State which cell type is depicted.
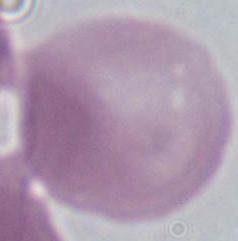
This is an erythrocyte.

Captured at 1000x magnification. Photomicrograph.